Outline each uninfected red blood cell.
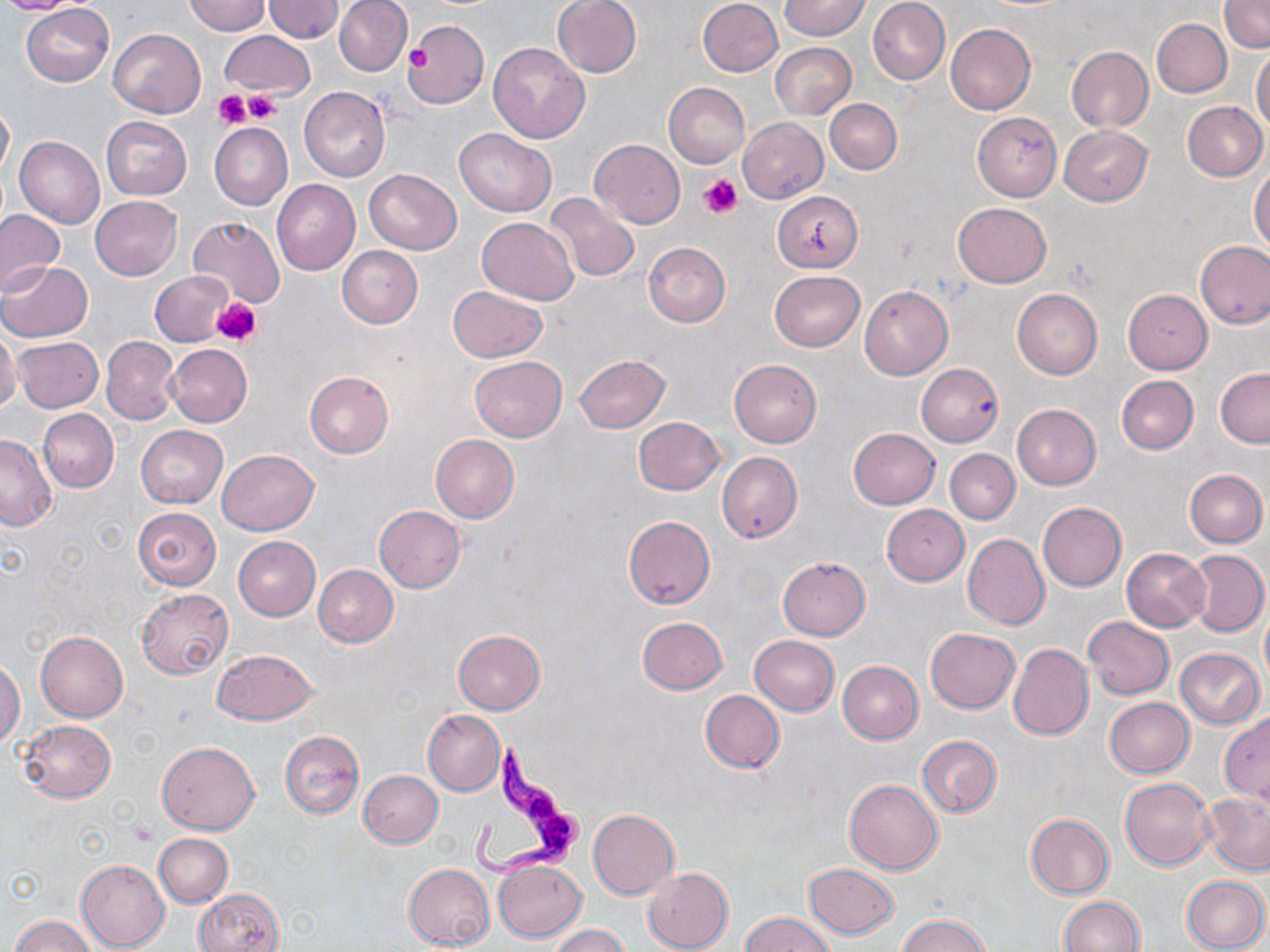
Approximate bounding boxes as (x1, y1, x2, y2) in pixels.
Uninfected red blood cells: (0, 0, 87, 15), (183, 0, 270, 35), (262, 0, 344, 42), (334, 0, 412, 76), (551, 0, 642, 77), (698, 0, 783, 77), (781, 0, 869, 40), (867, 0, 950, 85), (1219, 1, 1269, 53), (22, 3, 114, 86), (404, 19, 489, 109), (1152, 19, 1230, 98), (945, 24, 1035, 114), (107, 29, 205, 118), (220, 30, 314, 100), (488, 42, 590, 143), (770, 42, 856, 119), (1066, 47, 1153, 132), (1252, 47, 1270, 133), (663, 82, 750, 167), (299, 85, 391, 182), (824, 99, 901, 174), (0, 101, 13, 182), (1184, 101, 1268, 181), (972, 113, 1060, 200), (101, 117, 192, 199), (738, 117, 828, 203), (210, 123, 292, 210), (1059, 126, 1152, 206), (454, 127, 557, 216), (14, 137, 104, 230), (590, 139, 685, 229), (1250, 167, 1270, 250), (364, 170, 462, 253), (271, 178, 360, 274), (772, 190, 863, 272), (545, 193, 640, 281), (89, 196, 182, 280), (953, 203, 1052, 288), (0, 210, 65, 295), (187, 216, 284, 309), (477, 217, 578, 304), (1196, 240, 1270, 328), (643, 241, 730, 326), (337, 246, 422, 327), (1, 261, 92, 343), (769, 270, 865, 351), (151, 271, 235, 347), (448, 286, 548, 362), (860, 286, 952, 379), (1013, 288, 1102, 378), (1123, 289, 1214, 374), (0, 328, 21, 412), (12, 337, 104, 413), (101, 337, 178, 424), (166, 344, 251, 427), (574, 355, 671, 433), (470, 356, 566, 441), (729, 360, 821, 447), (916, 364, 1003, 447), (1216, 368, 1270, 447), (305, 372, 393, 459), (1116, 375, 1197, 454), (1011, 404, 1101, 490), (39, 409, 118, 492), (633, 417, 724, 495), (137, 425, 227, 507), (848, 428, 939, 510), (0, 433, 58, 530), (431, 435, 519, 523), (218, 449, 318, 535), (946, 449, 1019, 523), (717, 452, 802, 543), (1185, 469, 1267, 546), (1038, 502, 1127, 591), (881, 504, 968, 585), (374, 506, 465, 592), (132, 507, 222, 591), (623, 516, 715, 609), (963, 533, 1049, 630), (233, 536, 320, 620), (1122, 548, 1211, 632), (1186, 550, 1268, 636), (778, 557, 870, 640), (313, 565, 397, 647), (137, 589, 232, 678), (1263, 611, 1270, 682), (1083, 616, 1175, 699), (636, 617, 728, 695), (926, 628, 1019, 712), (454, 629, 545, 713), (37, 632, 128, 722), (751, 636, 840, 716), (1009, 644, 1094, 741), (1174, 647, 1265, 729), (213, 648, 318, 725), (0, 659, 23, 747), (837, 660, 923, 743), (701, 690, 783, 772), (1104, 697, 1194, 778), (424, 710, 505, 795), (1219, 713, 1270, 804), (19, 720, 115, 802), (279, 730, 364, 818), (917, 735, 1001, 817), (157, 741, 259, 835), (359, 770, 443, 848), (1119, 777, 1215, 870), (846, 779, 942, 875), (1200, 792, 1270, 876), (588, 809, 679, 898), (1025, 812, 1114, 898), (154, 833, 232, 907), (76, 859, 169, 951), (494, 859, 585, 943), (403, 863, 493, 950), (804, 863, 899, 938), (642, 867, 733, 952), (1182, 874, 1269, 952), (194, 888, 284, 952), (1058, 896, 1145, 951), (740, 912, 838, 952), (897, 914, 993, 952), (9, 916, 96, 952), (551, 925, 630, 952).

Trypanosoma brucei locations: (468, 743, 591, 886). Platelet locations: (405, 41, 434, 71), (213, 89, 253, 129), (243, 91, 281, 123), (700, 174, 742, 218), (212, 297, 262, 347). Slide-level diagnosis: Trypanosoma brucei. Image is 1270×952 pixels. One field of a larger specimen. Optical microscopy. Thin blood film. May-Grünwald-Giemsa stain. Captured at 1000x magnification.